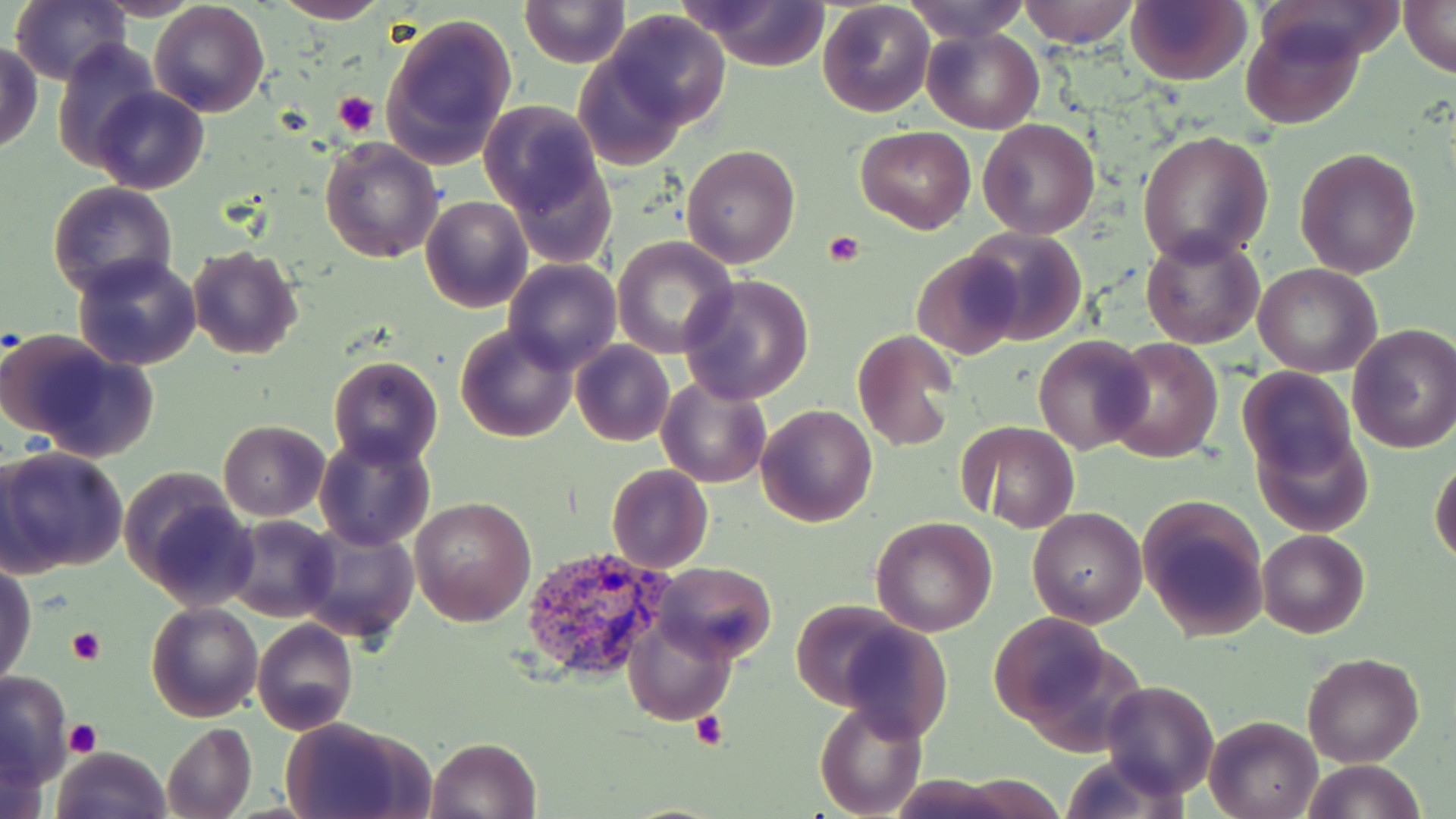

slide-level diagnosis = Plasmodium vivax
stain = May-Grünwald-Giemsa
platelet locations = approximate bounding boxes as named x1/y1/x2/y2 corners in pixels: (x1=334, y1=90, x2=378, y2=134), (x1=822, y1=231, x2=867, y2=267), (x1=68, y1=626, x2=105, y2=665), (x1=691, y1=710, x2=729, y2=750), (x1=65, y1=719, x2=103, y2=756)
magnification = 1000x
image size = 1456×819 pixels
modality = light microscopy
Plasmodium vivax-infected red blood cell locations = approximate bounding boxes as named x1/y1/x2/y2 corners in pixels: (x1=521, y1=545, x2=674, y2=682)
uninfected red blood cell locations = approximate bounding boxes as named x1/y1/x2/y2 corners in pixels: (x1=11, y1=0, x2=128, y2=86), (x1=93, y1=0, x2=207, y2=20), (x1=271, y1=0, x2=390, y2=24), (x1=521, y1=0, x2=630, y2=67), (x1=902, y1=0, x2=1031, y2=43), (x1=1018, y1=0, x2=1137, y2=48), (x1=1125, y1=0, x2=1250, y2=86), (x1=1400, y1=0, x2=1454, y2=76), (x1=148, y1=1, x2=270, y2=117), (x1=683, y1=1, x2=834, y2=70), (x1=817, y1=1, x2=935, y2=118), (x1=604, y1=10, x2=731, y2=127), (x1=379, y1=12, x2=517, y2=169), (x1=1240, y1=16, x2=1364, y2=130), (x1=921, y1=26, x2=1045, y2=133), (x1=53, y1=40, x2=162, y2=173), (x1=1, y1=44, x2=43, y2=155), (x1=572, y1=57, x2=690, y2=169), (x1=92, y1=87, x2=208, y2=195), (x1=479, y1=102, x2=605, y2=220), (x1=434, y1=119, x2=576, y2=279), (x1=978, y1=119, x2=1101, y2=239), (x1=854, y1=125, x2=976, y2=234), (x1=1138, y1=129, x2=1275, y2=267), (x1=319, y1=137, x2=445, y2=263), (x1=680, y1=143, x2=800, y2=268), (x1=1294, y1=148, x2=1422, y2=280), (x1=505, y1=154, x2=617, y2=266), (x1=47, y1=181, x2=179, y2=302), (x1=422, y1=193, x2=532, y2=313), (x1=963, y1=227, x2=1086, y2=347), (x1=1140, y1=230, x2=1265, y2=350), (x1=611, y1=235, x2=737, y2=358), (x1=186, y1=246, x2=305, y2=362), (x1=912, y1=248, x2=1025, y2=359), (x1=71, y1=253, x2=203, y2=370), (x1=503, y1=258, x2=623, y2=373), (x1=1253, y1=263, x2=1384, y2=378), (x1=679, y1=274, x2=814, y2=405), (x1=453, y1=323, x2=580, y2=443), (x1=1348, y1=323, x2=1456, y2=454), (x1=852, y1=328, x2=958, y2=451), (x1=1033, y1=334, x2=1153, y2=457), (x1=1106, y1=336, x2=1222, y2=464), (x1=12, y1=337, x2=158, y2=460), (x1=570, y1=341, x2=674, y2=447), (x1=328, y1=357, x2=441, y2=468), (x1=1237, y1=368, x2=1359, y2=480), (x1=656, y1=375, x2=773, y2=489), (x1=756, y1=404, x2=878, y2=528), (x1=218, y1=420, x2=331, y2=521), (x1=957, y1=420, x2=1081, y2=532), (x1=1255, y1=426, x2=1373, y2=538), (x1=316, y1=433, x2=434, y2=551), (x1=0, y1=446, x2=129, y2=576), (x1=1430, y1=454, x2=1456, y2=569), (x1=606, y1=464, x2=713, y2=573), (x1=120, y1=473, x2=257, y2=609), (x1=408, y1=495, x2=536, y2=626), (x1=1138, y1=495, x2=1271, y2=642), (x1=1026, y1=507, x2=1147, y2=629), (x1=225, y1=515, x2=340, y2=622), (x1=870, y1=516, x2=998, y2=637), (x1=295, y1=517, x2=418, y2=645), (x1=1257, y1=530, x2=1369, y2=639), (x1=1, y1=560, x2=36, y2=689), (x1=651, y1=561, x2=776, y2=664), (x1=791, y1=599, x2=914, y2=709), (x1=145, y1=601, x2=264, y2=722), (x1=990, y1=613, x2=1120, y2=735), (x1=624, y1=616, x2=736, y2=726), (x1=252, y1=619, x2=358, y2=735), (x1=835, y1=621, x2=953, y2=743), (x1=1302, y1=651, x2=1424, y2=767), (x1=0, y1=668, x2=72, y2=788), (x1=1100, y1=681, x2=1220, y2=800), (x1=815, y1=699, x2=926, y2=818), (x1=280, y1=715, x2=434, y2=819), (x1=1205, y1=716, x2=1322, y2=819), (x1=161, y1=721, x2=256, y2=819), (x1=426, y1=736, x2=544, y2=819), (x1=51, y1=746, x2=171, y2=819), (x1=1301, y1=757, x2=1425, y2=819), (x1=942, y1=774, x2=1072, y2=816)
field of view = single
preparation = thin blood film